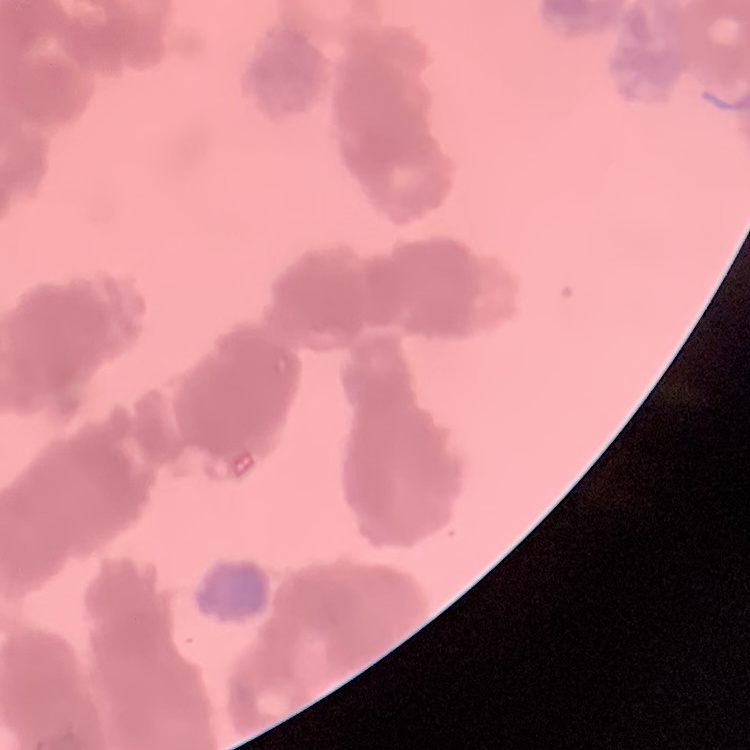
red blood cell morphology = rouleaux formation
image type = one tile cut from a larger photomicrograph
preparation = thin peripheral smear
stain = Field's or Giemsa